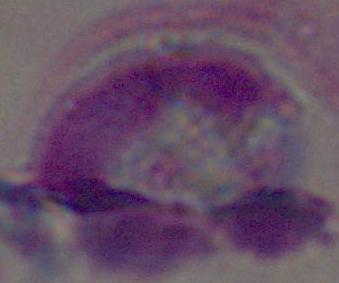
Summary:
  - Identification: white blood cell
  - Magnification: 1000x
  - Modality: micrograph